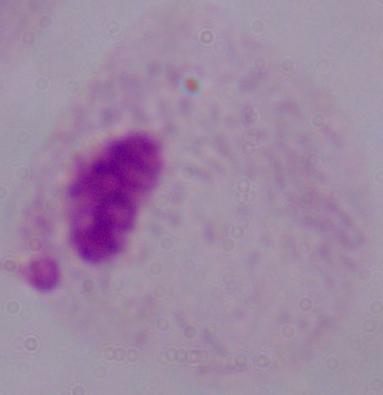
Summary:
  - Modality: micrograph
  - Identification: trichomonad
  - Magnification: 1000x